Describe the morphology of the erythrocytes.
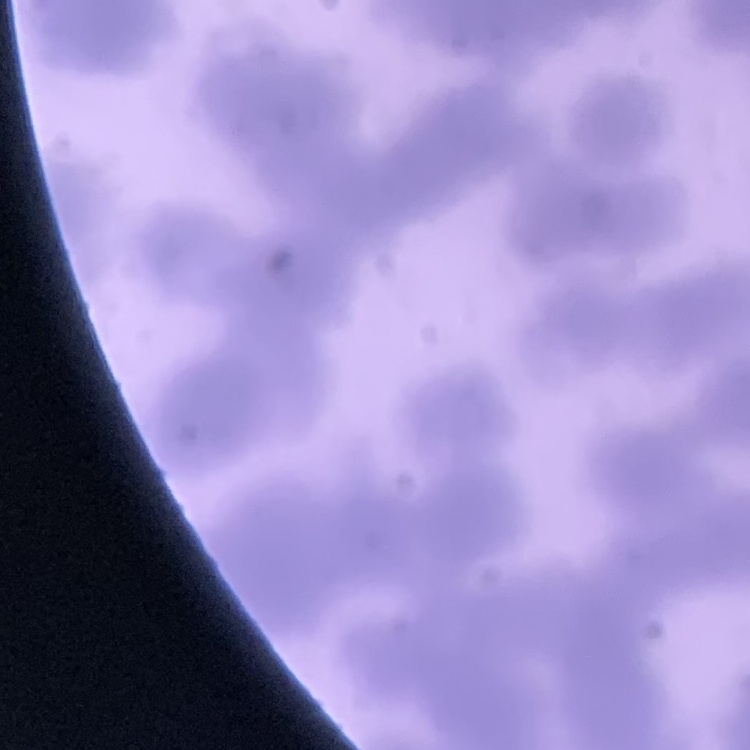
They show rouleaux formation.

Square crop of a larger photomicrograph. Field's or Giemsa stain. Thin blood smear.